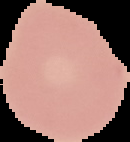
{
  "preparation": "thin blood film",
  "image_size": "130×142 pixels",
  "malaria_status": "uninfected",
  "image_type": "cell region segmented out of the field of view; surrounding area masked to black"
}